Give the preparation type.
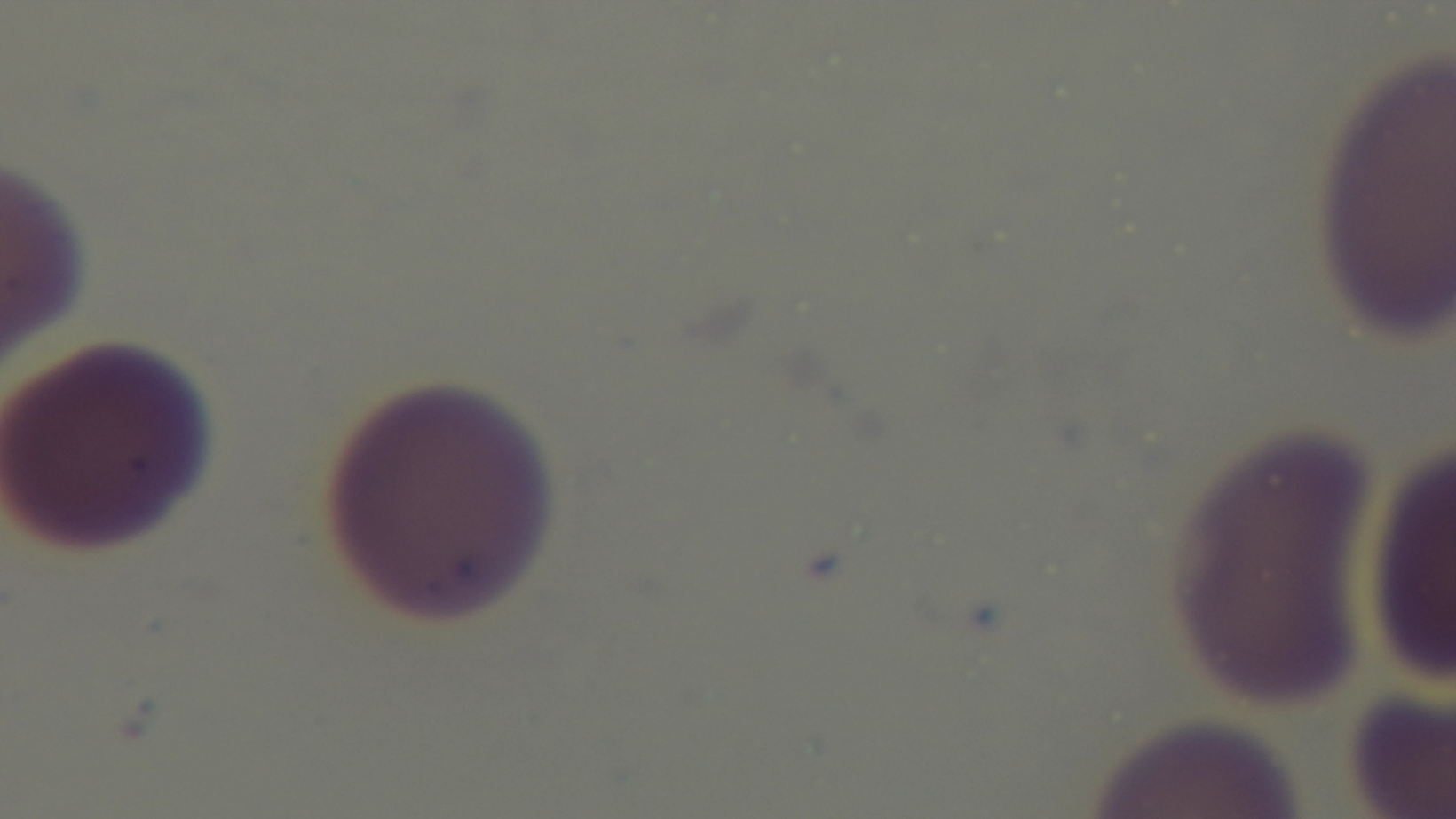

A thin smear.

Malaria status: uninfected. Giemsa stain. Mounted 4K digital camera. 100x oil-immersion objective. Single field of view. Photomicrograph.